Locate and identify every blood parasite.
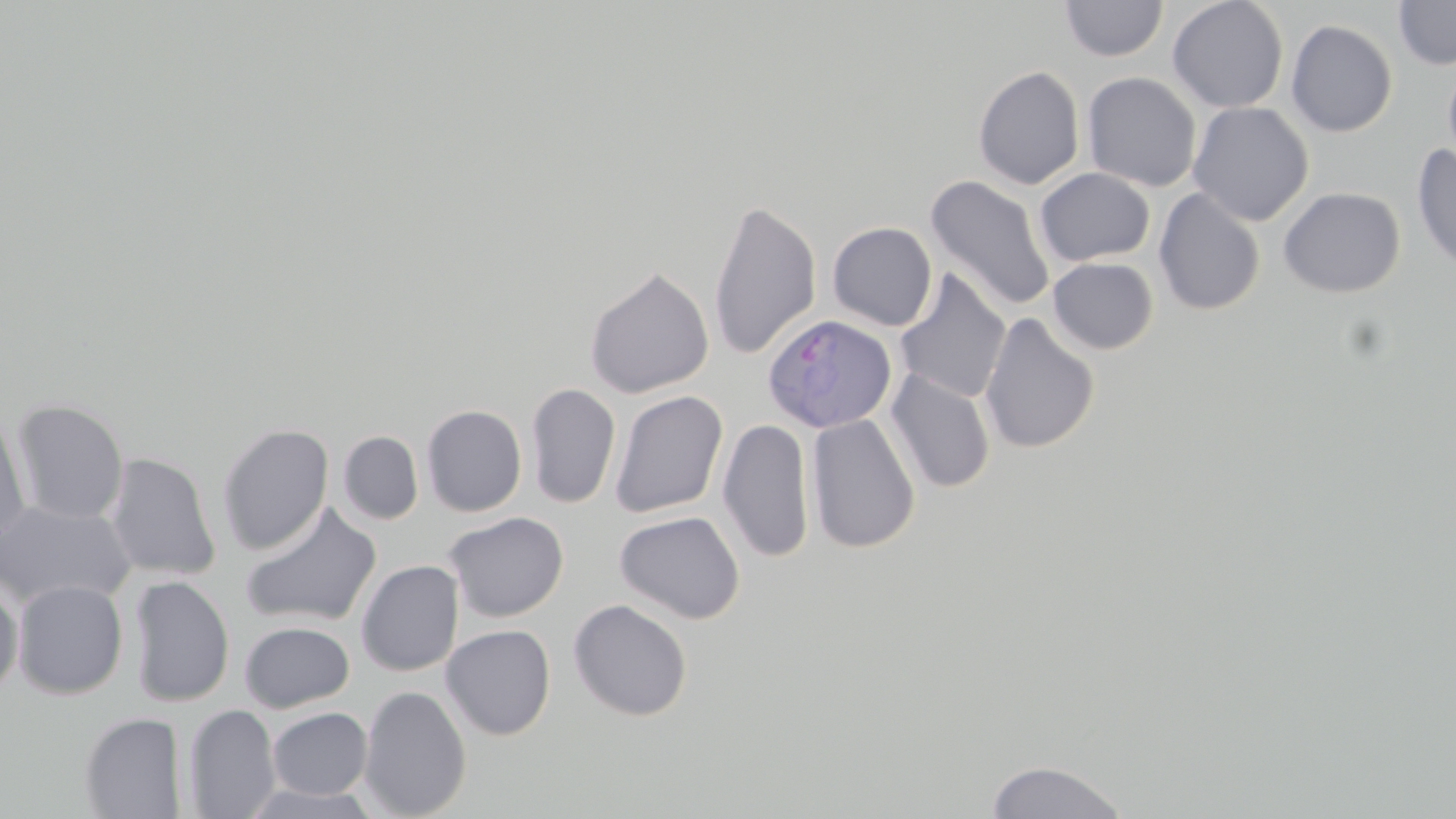

Approximate bounding boxes as (x1, y1, x2, y2) in pixels.
Plasmodium ovale-infected red blood cells: (763, 312, 897, 434).
No Plasmodium falciparum, Plasmodium malariae, Plasmodium vivax, Babesia divergens, or Trypanosoma brucei observed.

Uninfected red blood cell locations: (1060, 0, 1168, 62), (1167, 0, 1289, 113), (1393, 0, 1456, 69), (1170, 12, 1401, 124), (1285, 19, 1398, 137), (1443, 59, 1456, 172), (973, 66, 1085, 190), (1082, 72, 1202, 192), (1187, 101, 1314, 226), (1411, 144, 1456, 273), (1034, 167, 1156, 267), (925, 174, 1055, 313), (1278, 186, 1406, 297), (1153, 187, 1265, 315), (707, 196, 822, 361), (827, 221, 937, 331), (1048, 257, 1159, 354), (584, 266, 714, 399), (894, 269, 1012, 405), (979, 311, 1100, 455), (885, 369, 995, 493), (526, 382, 621, 509), (610, 389, 728, 518), (10, 399, 129, 525), (421, 405, 527, 517), (0, 409, 31, 549), (806, 413, 921, 554), (718, 416, 816, 563), (216, 422, 335, 556), (338, 431, 424, 524), (104, 452, 221, 581), (0, 500, 135, 609), (240, 502, 382, 629), (615, 510, 746, 624), (444, 511, 569, 623), (356, 560, 464, 677), (127, 575, 235, 707), (0, 579, 24, 698), (11, 579, 129, 700), (567, 599, 693, 722), (239, 621, 355, 713), (441, 624, 556, 740), (358, 685, 472, 818), (183, 703, 281, 819), (267, 707, 373, 800), (79, 712, 187, 818), (985, 759, 1128, 818). Slide-level diagnosis: Plasmodium ovale. Captured at 1000x magnification. Thin blood smear. One field of a larger specimen. Image is 1456×819 pixels. Optical microscopy. May-Grünwald-Giemsa stain.